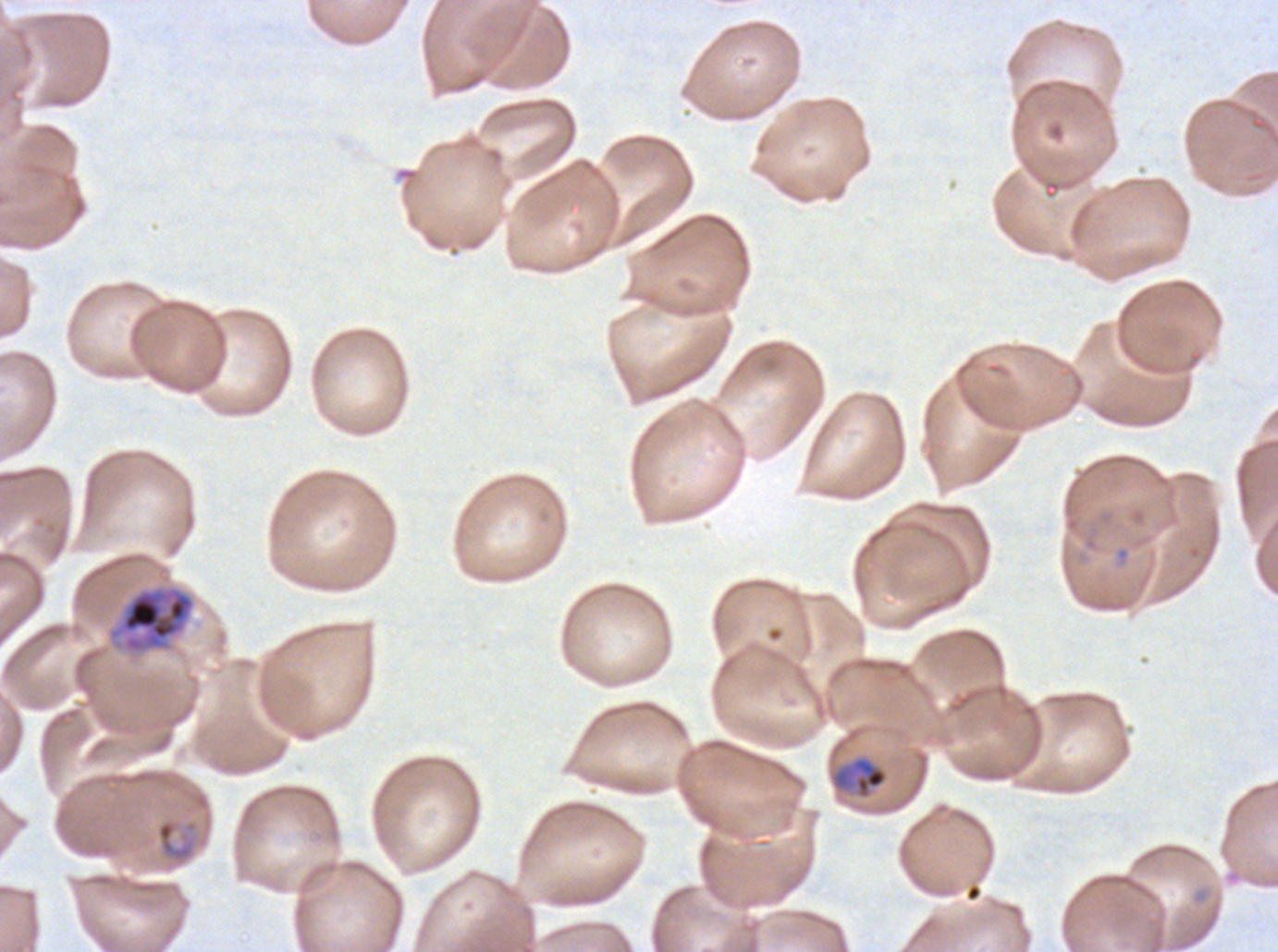
Approximate bounding boxes as [x1, y1, x2, y2] in pixels. Late trophozoite locations: [107, 585, 196, 655]. Mid trophozoite locations: [831, 756, 889, 799]. Late-ring/early-trophozoite locations: [154, 817, 200, 866]. Ex-vivo Plasmodium falciparum culture from a patient in The Gambia, grown for 24 to 48 hours. Giemsa stain. Thin blood film. A sub-image separated from a larger composite. Image is 1278×952 pixels. Life-cycle stages observed: late-ring/early-trophozoite, mid trophozoite, late trophozoite.